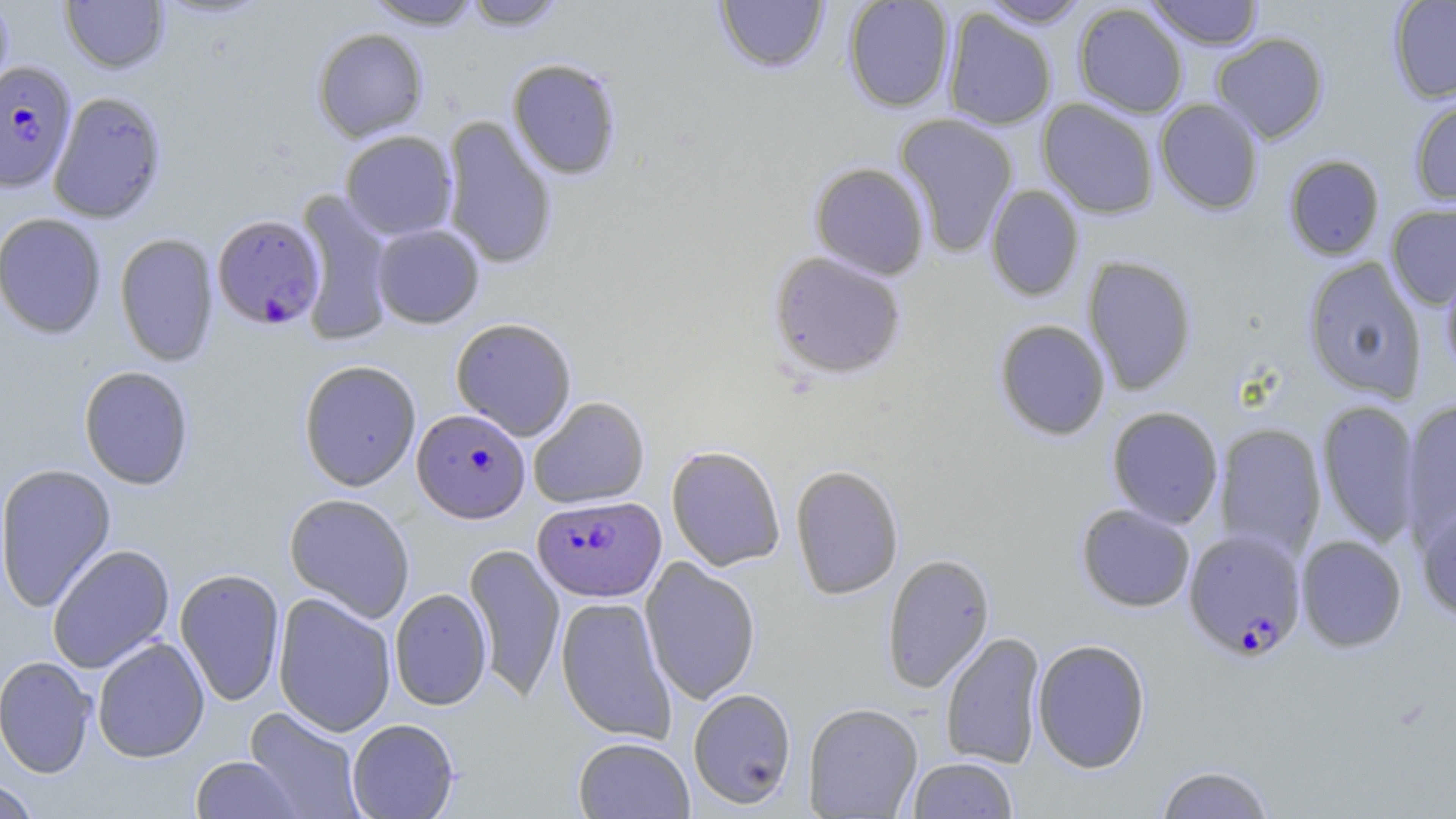

slide-level diagnosis = Plasmodium falciparum
stain = May-Grünwald-Giemsa
Plasmodium falciparum-infected red blood cell locations = approximate bounding boxes as (x1, y1, x2, y2) in pixels: (0, 62, 76, 192), (211, 214, 324, 330), (412, 408, 530, 523), (532, 495, 665, 602), (1184, 528, 1307, 661)
uninfected red blood cell locations = approximate bounding boxes as (x1, y1, x2, y2) in pixels: (0, 0, 14, 101), (60, 0, 169, 74), (154, 0, 274, 23), (364, 0, 484, 29), (461, 0, 567, 31), (715, 0, 829, 74), (842, 0, 955, 113), (979, 0, 1091, 27), (1144, 0, 1265, 50), (1388, 1, 1456, 103), (1072, 3, 1189, 118), (942, 9, 1057, 130), (311, 28, 429, 142), (1211, 32, 1329, 144), (507, 58, 622, 180), (48, 91, 167, 224), (1408, 96, 1456, 206), (1037, 98, 1159, 218), (1154, 98, 1263, 215), (894, 113, 1019, 257), (441, 115, 558, 270), (339, 130, 457, 240), (1283, 154, 1385, 260), (809, 162, 930, 280), (985, 184, 1084, 302), (295, 188, 395, 347), (1386, 202, 1456, 310), (1, 213, 107, 339), (371, 224, 484, 328), (1, 225, 218, 347), (114, 232, 219, 367), (768, 251, 907, 379), (1082, 255, 1197, 395), (1302, 257, 1427, 403), (1441, 263, 1456, 379), (450, 317, 578, 440), (994, 319, 1111, 440), (298, 359, 421, 492), (78, 366, 194, 490), (528, 396, 650, 508), (1316, 399, 1421, 548), (1401, 399, 1456, 544), (1106, 406, 1224, 528), (1214, 423, 1327, 560), (666, 444, 785, 571), (0, 463, 117, 612), (789, 464, 904, 600), (284, 493, 415, 622), (1415, 502, 1456, 621), (1076, 504, 1196, 612), (1296, 535, 1407, 652), (464, 542, 566, 703), (46, 544, 174, 673), (881, 552, 995, 693), (640, 557, 761, 705), (174, 567, 285, 706), (389, 588, 492, 710), (273, 593, 397, 736), (555, 596, 677, 743), (940, 631, 1046, 769), (92, 636, 210, 763), (1032, 638, 1151, 773), (0, 656, 97, 778), (688, 687, 797, 809), (803, 702, 923, 817), (243, 706, 367, 819), (347, 718, 459, 818), (573, 736, 694, 819), (190, 755, 304, 818), (907, 757, 1018, 818), (1155, 764, 1275, 818), (0, 777, 41, 818)
magnification = 1000x
modality = light microscopy
field of view = single
preparation = thin blood film
image size = 1456×819 pixels